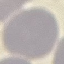
Summary:
  - Malaria status: uninfected
  - Preparation: thin blood film
  - Stain: Giemsa
  - Capture: smartphone through the microscope eyepiece
  - Image type: cell patch, automatically extracted from a larger field of view and resized to 64 × 64 pixels